Name the parasite shown.
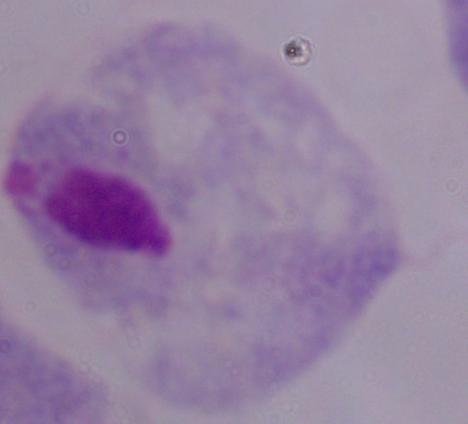

A trichomonad.

Summary:
  - Magnification: 1000x
  - Modality: photomicrograph